Report the malaria status of this cell.
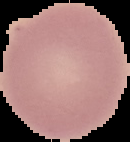
It is uninfected.

From a thin blood smear. Segmented cell region on a black background. Image is 130×142 pixels.